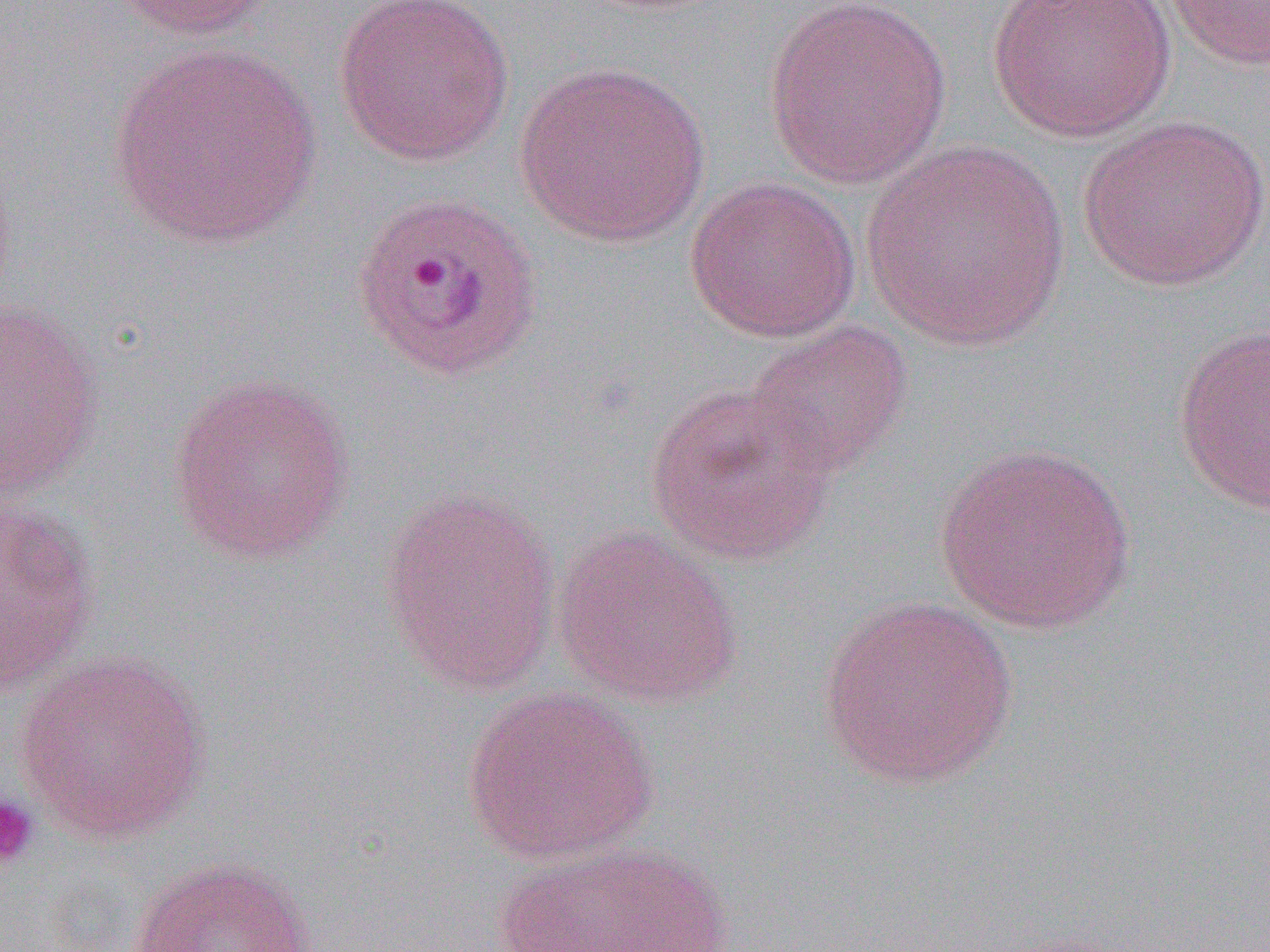
Plasmodium ovale-infected red blood cell locations = approximate bounding boxes as (x1, y1, x2, y2) in pixels: (349, 190, 546, 382)
slide-level diagnosis = Plasmodium ovale
magnification = 1000x
preparation = thin blood smear
image size = 1270×952 pixels
modality = optical microscopy
platelet locations = approximate bounding boxes as (x1, y1, x2, y2) in pixels: (0, 793, 39, 871)
uninfected red blood cell locations = approximate bounding boxes as (x1, y1, x2, y2) in pixels: (105, 0, 275, 39), (332, 0, 516, 167), (762, 0, 951, 188), (987, 0, 1177, 143), (1163, 0, 1270, 72), (107, 43, 323, 249), (515, 60, 711, 248), (1076, 115, 1268, 292), (860, 140, 1071, 352), (684, 175, 861, 343), (0, 299, 106, 501), (741, 319, 914, 482), (1172, 323, 1270, 516), (166, 371, 357, 563), (645, 381, 840, 567), (934, 441, 1138, 635), (379, 488, 562, 694), (0, 500, 102, 693), (551, 525, 744, 706), (815, 595, 1017, 790), (15, 651, 214, 846), (461, 685, 661, 866), (496, 839, 732, 952), (126, 855, 319, 952)
field of view = one of a larger specimen